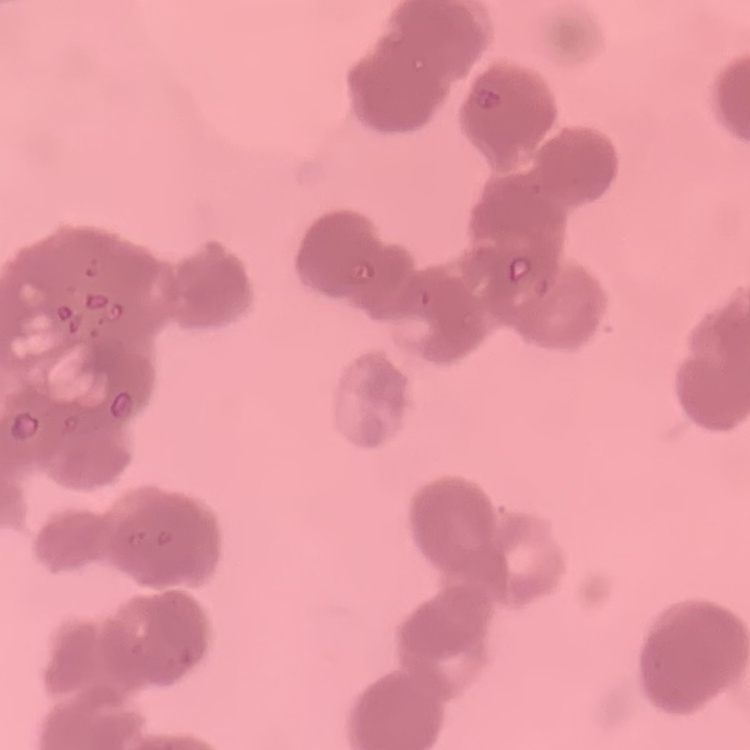

The erythrocytes exhibit rouleaux formation. Stained with either Field's or Giemsa. Square crop of a larger photomicrograph. Thin blood smear.